Assess the morphology of the erythrocytes.
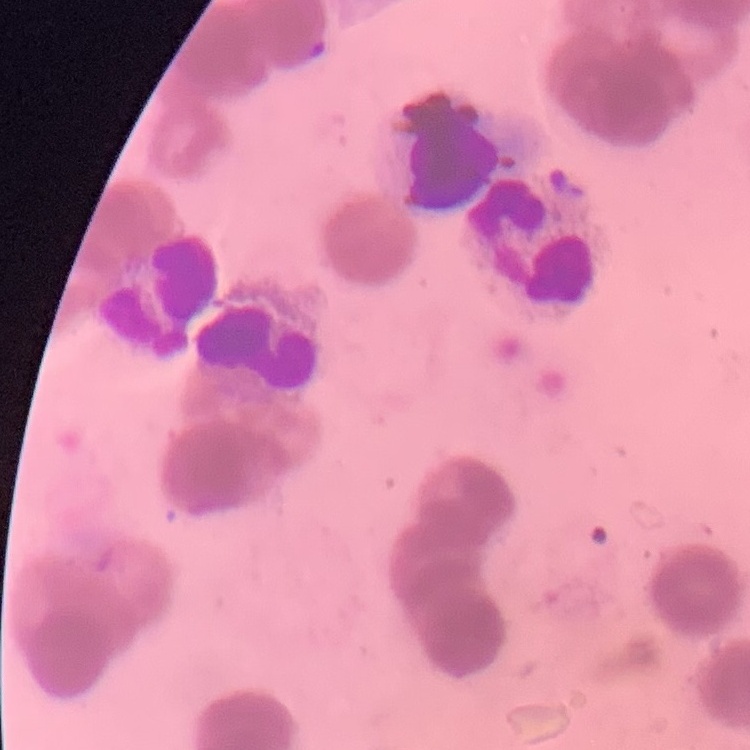

Rouleaux formation.

Summary:
  - Preparation: thin blood smear
  - Image type: one tile cut from a larger photomicrograph
  - Stain: Field's or Giemsa